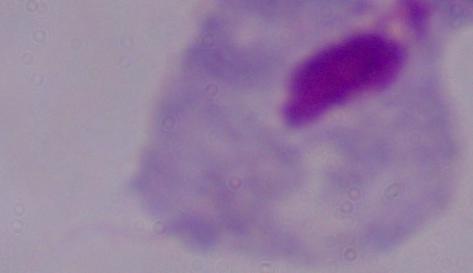

{
  "identification": "trichomonad",
  "magnification": "1000x",
  "modality": "photomicrograph"
}